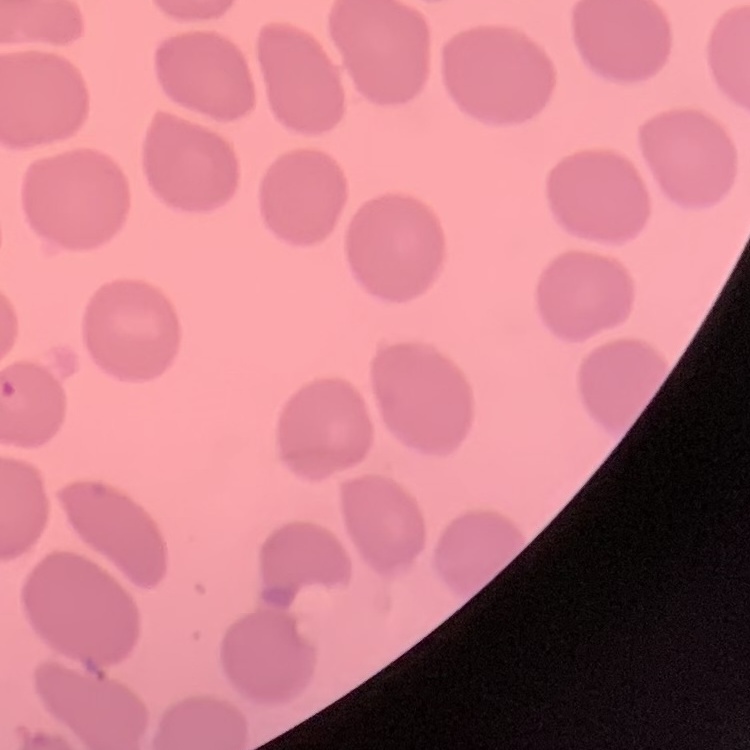
erythrocyte morphology = no rouleaux formation
stain = Field's or Giemsa
preparation = thin blood smear
image type = square crop of a larger photomicrograph